Classify this cell by malaria status.
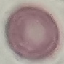

It is uninfected.

Photographed with a smartphone camera at the microscope eyepiece. Giemsa-stained preparation. Thin blood film. Automatically extracted cell patch, resized to 64 × 64 pixels.